Locate every Plasmodium falciparum parasite and give its life-cycle stage, and locate every leukocyte and any debris.
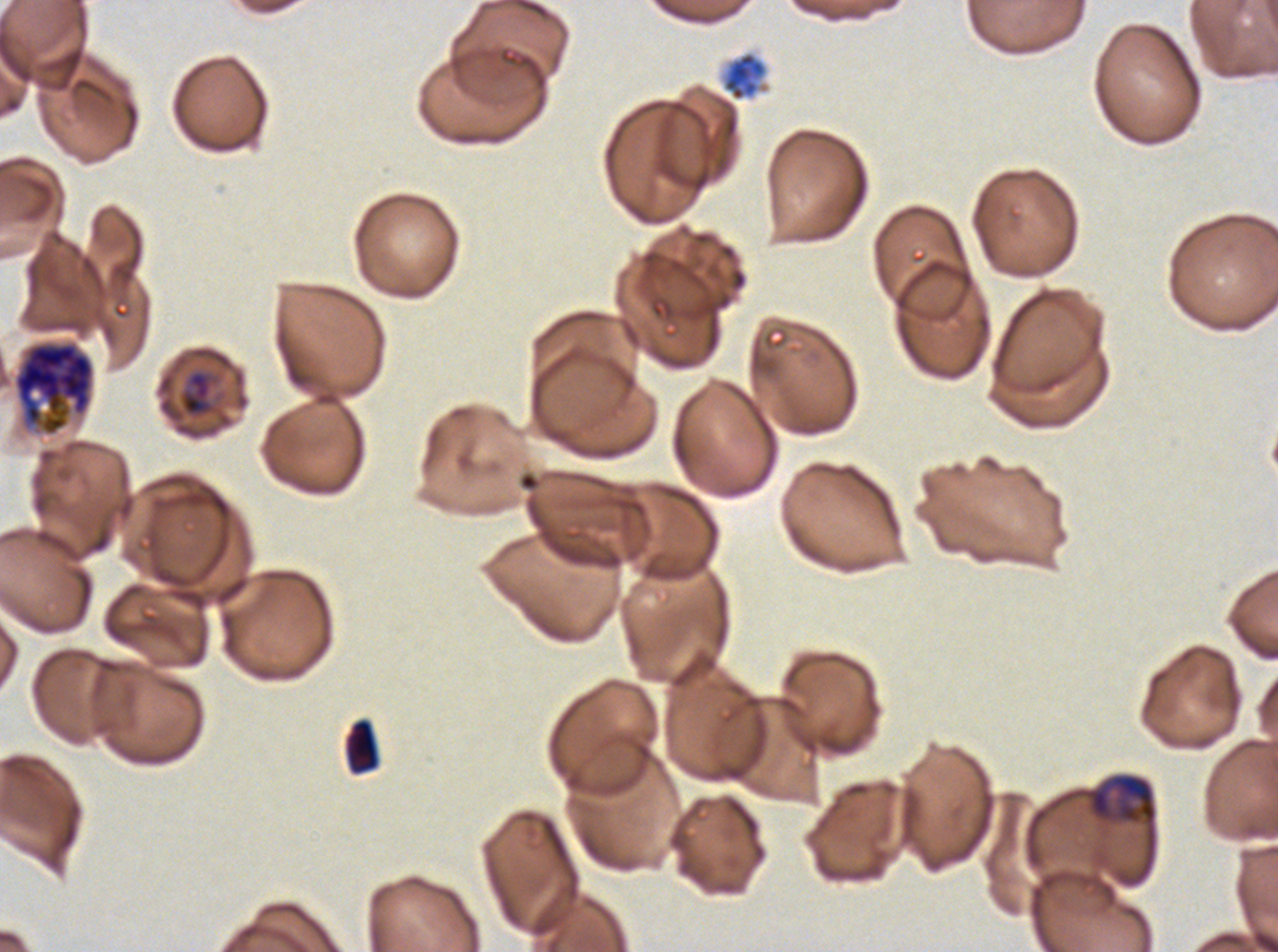

Approximate bounding boxes as [x1, y1, x2, y2] in pixels.
Late-ring/early-trophozoite forms: [179, 371, 213, 417].
Mid trophozoites: [1086, 773, 1158, 827].
Late schizonts: [12, 340, 95, 437].
Segmenters: [601, 50, 768, 200].
Debris: [343, 717, 380, 775].
No rings, late trophozoites, early schizonts, gametocytes, or leukocytes observed.

Summary:
  - Preparation: thin blood film
  - Field of view: sub-image separated from a larger composite
  - Specimen: Plasmodium falciparum cultured ex vivo for 24 to 48 hours, from a patient in The Gambia
  - Life-cycle stages observed: late-ring/early-trophozoite, mid trophozoite, late schizont, segmenter
  - Image size: 1278×952 pixels
  - Stain: Giemsa